Locate every malaria parasite.
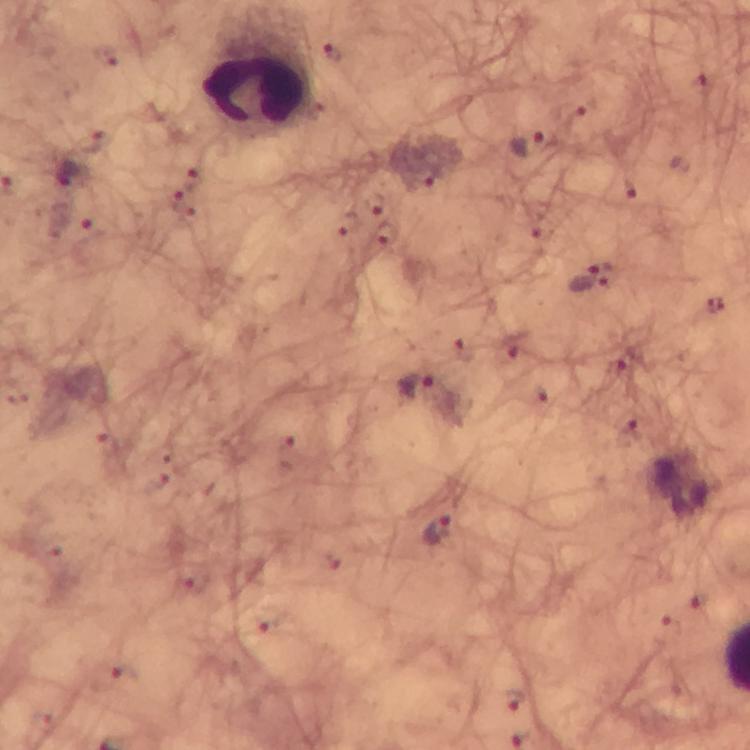

Approximate object centers, in pixels from the top-left corner.
Malaria parasites: (x=333, y=53), (x=576, y=124), (x=525, y=145), (x=69, y=175), (x=427, y=175), (x=630, y=188), (x=181, y=203), (x=373, y=204), (x=385, y=232), (x=608, y=275), (x=579, y=277), (x=512, y=345), (x=626, y=359), (x=418, y=387), (x=629, y=435), (x=288, y=453), (x=437, y=532), (x=513, y=701).

Leukocyte locations: (x=256, y=88). Smartphone photograph taken through a microscope. Immersion oil was used. From a diagnostic examination for malaria. 100x magnification. Cropped region of a single field of view. Giemsa stain. Thick blood smear. Image is 750×750 pixels.